Report the malaria status of this cell.
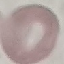

Uninfected.

Summary:
  - Capture: smartphone through the microscope eyepiece
  - Image type: cell patch, automatically extracted from a larger field of view and resized to 64 × 64 pixels
  - Preparation: thin smear
  - Stain: Giemsa